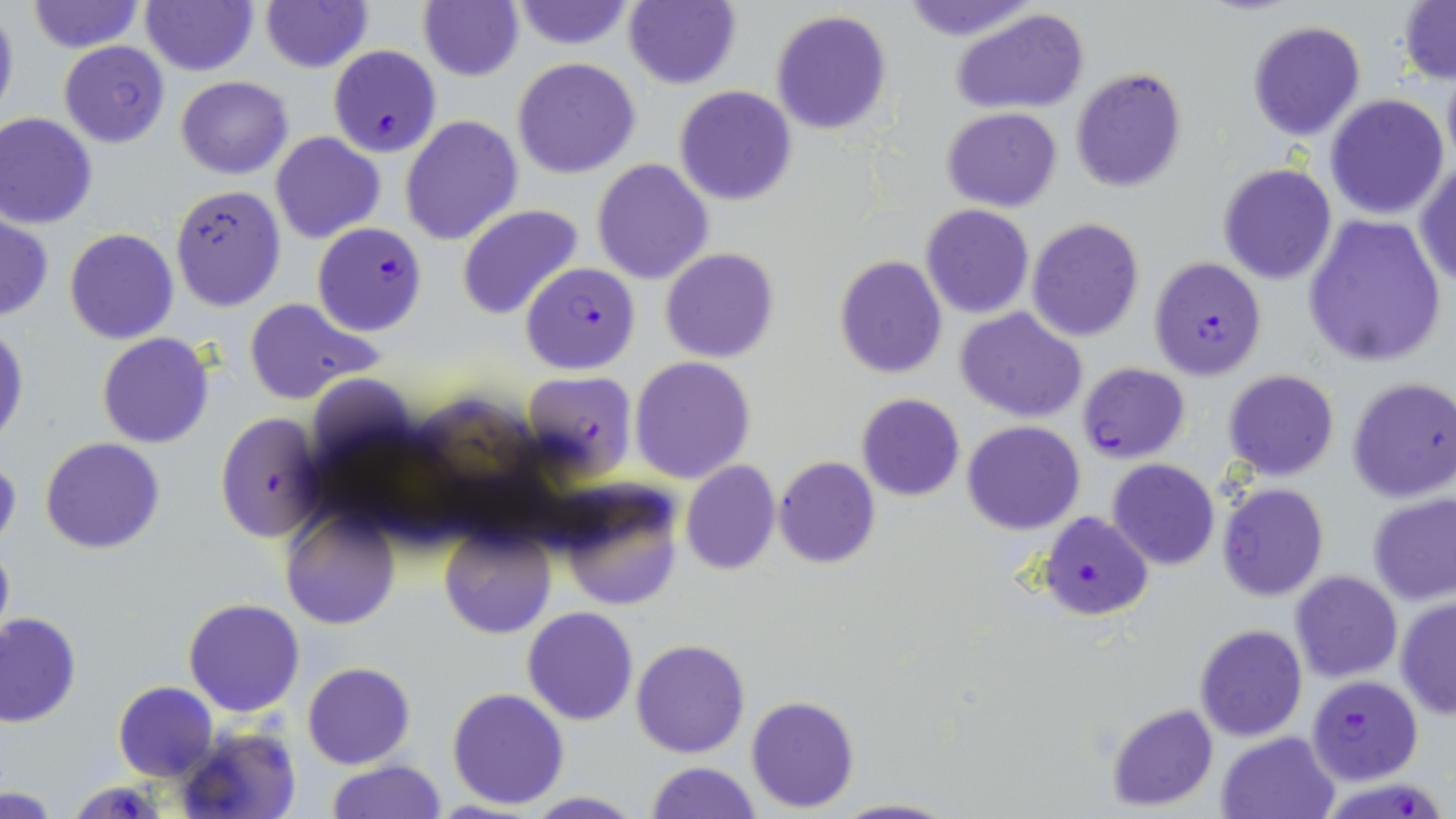

Approximate bounding boxes as (x1, y1, x2, y2) in pixels. Uninfected red blood cell locations: (25, 0, 143, 55), (140, 0, 258, 75), (417, 0, 523, 83), (623, 0, 740, 90), (897, 0, 1040, 41), (1399, 0, 1455, 84), (508, 1, 637, 51), (260, 2, 371, 73), (0, 5, 19, 125), (951, 5, 1089, 114), (769, 9, 893, 135), (1246, 20, 1367, 141), (58, 40, 171, 147), (512, 57, 641, 179), (1070, 66, 1187, 194), (1441, 70, 1456, 168), (175, 75, 292, 179), (674, 85, 798, 205), (1324, 93, 1450, 221), (941, 107, 1062, 211), (1, 112, 98, 229), (400, 115, 522, 247), (270, 131, 385, 244), (590, 158, 714, 285), (1413, 159, 1456, 289), (1216, 162, 1338, 285), (169, 185, 287, 311), (920, 203, 1034, 319), (458, 204, 584, 321), (1301, 213, 1446, 367), (0, 215, 52, 322), (1027, 217, 1145, 341), (64, 228, 179, 344), (662, 248, 780, 363), (833, 254, 948, 379), (243, 297, 383, 405), (957, 307, 1088, 423), (0, 323, 28, 446), (96, 332, 215, 448), (630, 356, 756, 484), (1222, 369, 1340, 481), (1348, 376, 1456, 502), (855, 393, 965, 501), (962, 421, 1085, 535), (41, 437, 165, 554), (0, 455, 21, 551), (773, 457, 881, 569), (679, 459, 780, 576), (1106, 459, 1220, 570), (1216, 483, 1329, 601), (553, 484, 685, 613), (1367, 491, 1456, 604), (279, 505, 401, 631), (439, 524, 556, 640), (0, 538, 14, 649), (1290, 571, 1403, 683), (182, 597, 305, 718), (1395, 598, 1455, 720), (522, 607, 638, 726), (0, 612, 80, 727), (1193, 624, 1307, 742), (631, 638, 751, 759), (302, 661, 416, 769), (113, 681, 219, 782), (445, 687, 569, 810), (744, 695, 860, 813), (1106, 702, 1219, 812), (174, 726, 303, 819), (1216, 730, 1340, 819), (326, 760, 446, 818), (645, 761, 762, 818), (3, 786, 63, 817), (519, 791, 645, 818), (834, 797, 957, 818). Plasmodium falciparum-infected red blood cell locations: (327, 45, 442, 158), (312, 220, 428, 336), (1147, 256, 1268, 380), (520, 263, 641, 376), (1076, 362, 1190, 464), (519, 370, 639, 481), (214, 412, 326, 542), (1038, 510, 1153, 620), (1308, 674, 1421, 784), (63, 782, 168, 817), (1327, 788, 1444, 819). Slide-level diagnosis: Plasmodium falciparum. Optical microscopy. May-Grünwald-Giemsa-stained preparation. Thin blood smear. 1000x magnification. Image is 1456×819 pixels. One field of a larger specimen.